Report the malaria status of this cell.
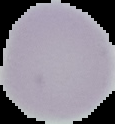

It is uninfected.

From a thin blood smear. Cell region segmented out of the field of view; the surrounding area is masked to black. Image is 115×124 pixels.